Outline each Plasmodium falciparum-infected red blood cell.
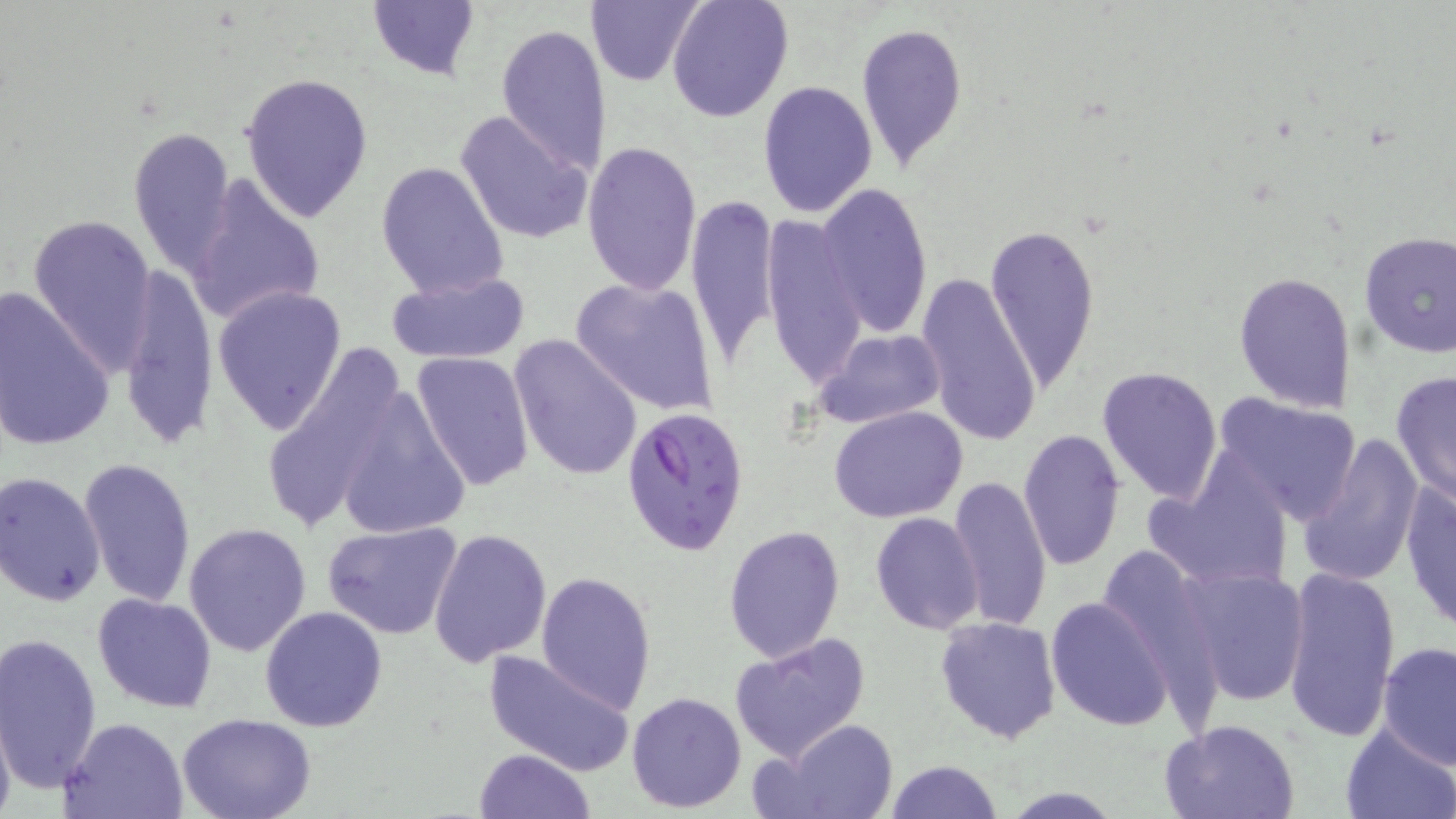
Approximate bounding boxes as named x1/y1/x2/y2 corners in pixels.
Plasmodium falciparum-infected red blood cells: (x1=619, y1=406, x2=751, y2=555).

Summary:
  - Uninfected red blood cell locations: (x1=584, y1=0, x2=704, y2=88), (x1=665, y1=0, x2=794, y2=123), (x1=366, y1=1, x2=482, y2=81), (x1=855, y1=19, x2=967, y2=171), (x1=494, y1=22, x2=613, y2=177), (x1=240, y1=71, x2=373, y2=223), (x1=757, y1=80, x2=878, y2=218), (x1=455, y1=109, x2=592, y2=246), (x1=128, y1=125, x2=237, y2=276), (x1=583, y1=140, x2=702, y2=298), (x1=375, y1=160, x2=510, y2=301), (x1=185, y1=174, x2=327, y2=326), (x1=816, y1=183, x2=933, y2=337), (x1=686, y1=194, x2=780, y2=372), (x1=28, y1=212, x2=158, y2=376), (x1=761, y1=215, x2=865, y2=391), (x1=986, y1=220, x2=1100, y2=398), (x1=1357, y1=231, x2=1456, y2=358), (x1=118, y1=268, x2=218, y2=454), (x1=387, y1=270, x2=531, y2=366), (x1=1232, y1=270, x2=1357, y2=413), (x1=915, y1=273, x2=1042, y2=448), (x1=569, y1=277, x2=720, y2=416), (x1=0, y1=284, x2=116, y2=453), (x1=212, y1=287, x2=347, y2=436), (x1=812, y1=327, x2=948, y2=430), (x1=509, y1=334, x2=642, y2=480), (x1=257, y1=343, x2=416, y2=536), (x1=410, y1=351, x2=535, y2=491), (x1=1097, y1=365, x2=1223, y2=505), (x1=1390, y1=371, x2=1456, y2=505), (x1=327, y1=374, x2=473, y2=545), (x1=1210, y1=391, x2=1361, y2=523), (x1=829, y1=406, x2=968, y2=524), (x1=1017, y1=429, x2=1126, y2=571), (x1=1296, y1=432, x2=1422, y2=587), (x1=78, y1=458, x2=197, y2=607), (x1=1142, y1=464, x2=1294, y2=593), (x1=1, y1=472, x2=106, y2=607), (x1=948, y1=474, x2=1053, y2=633), (x1=1399, y1=478, x2=1456, y2=635), (x1=870, y1=512, x2=986, y2=635), (x1=184, y1=521, x2=312, y2=656), (x1=321, y1=521, x2=463, y2=641), (x1=723, y1=525, x2=845, y2=662), (x1=427, y1=528, x2=553, y2=669), (x1=1097, y1=544, x2=1216, y2=684), (x1=1176, y1=560, x2=1312, y2=707), (x1=1280, y1=567, x2=1401, y2=746), (x1=535, y1=570, x2=658, y2=712), (x1=91, y1=592, x2=218, y2=712), (x1=1045, y1=597, x2=1173, y2=732), (x1=260, y1=606, x2=388, y2=733), (x1=935, y1=615, x2=1061, y2=743), (x1=0, y1=630, x2=102, y2=793), (x1=729, y1=630, x2=872, y2=763), (x1=1376, y1=640, x2=1456, y2=771), (x1=482, y1=650, x2=637, y2=777), (x1=626, y1=690, x2=747, y2=811), (x1=0, y1=709, x2=16, y2=819), (x1=176, y1=713, x2=317, y2=819), (x1=61, y1=717, x2=187, y2=819), (x1=1160, y1=717, x2=1302, y2=819), (x1=765, y1=719, x2=901, y2=819), (x1=1339, y1=724, x2=1454, y2=819), (x1=472, y1=748, x2=595, y2=819), (x1=884, y1=759, x2=1001, y2=819), (x1=1000, y1=788, x2=1123, y2=818)
  - Slide-level diagnosis: Plasmodium falciparum
  - Preparation: thin blood film
  - Magnification: 1000x
  - Modality: light microscopy
  - Field of view: one of a larger specimen
  - Stain: May-Grünwald-Giemsa
  - Image size: 1456×819 pixels